Locate every Plasmodium parasite.
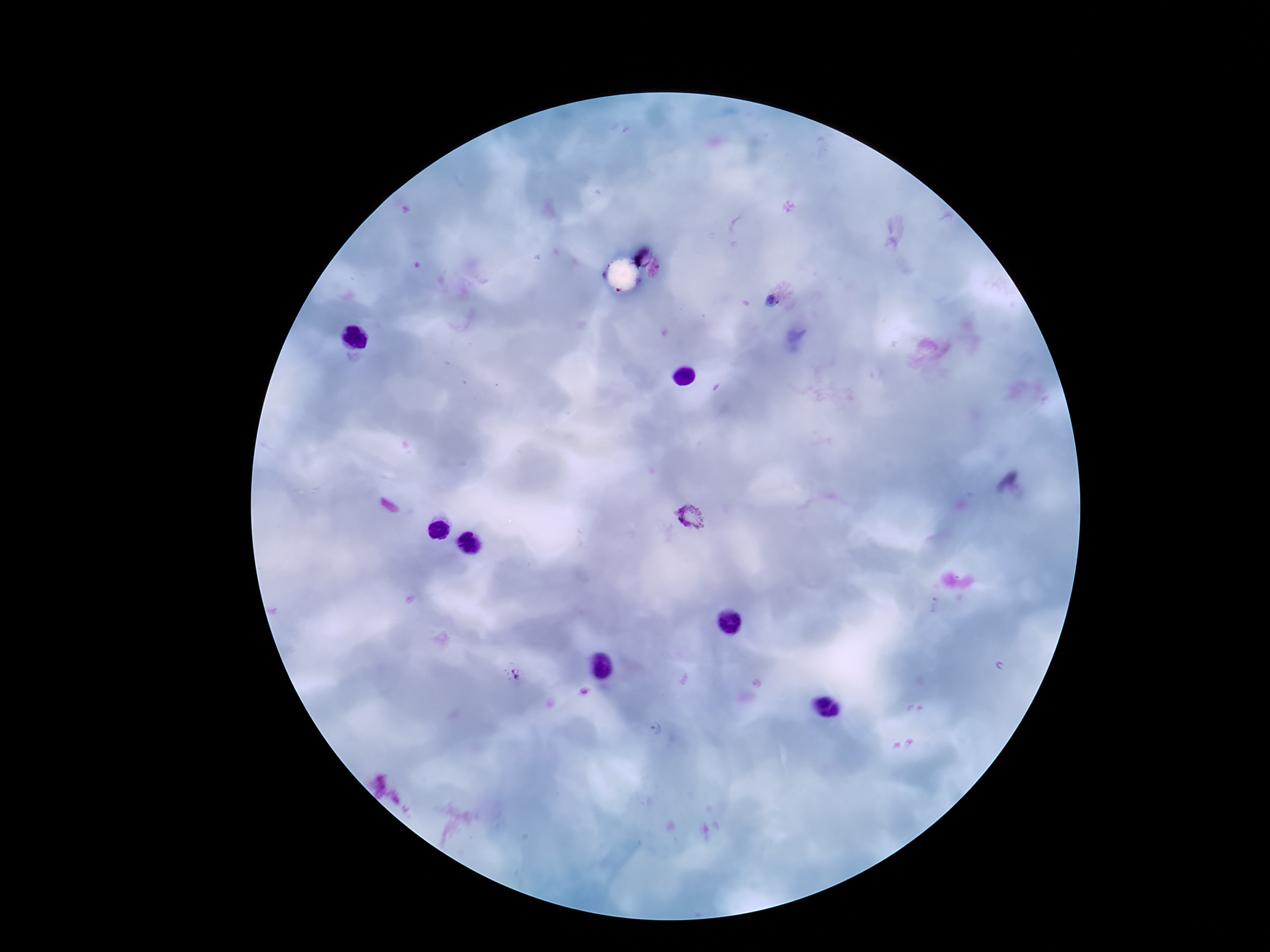

Approximate centers as (x, y) in pixels.
Plasmodium parasites: (690, 517), (935, 607), (1002, 666), (515, 676), (655, 729).

{
  "magnification": "100x",
  "stain": "Giemsa",
  "field_of_view": "one from this slide",
  "preparation": "thick peripheral-blood smear",
  "patient_malaria_status": "infected",
  "capture": "smartphone camera through the microscope eyepiece",
  "image_size": "1270×952 pixels"
}